Outline each blood parasite and name the species.
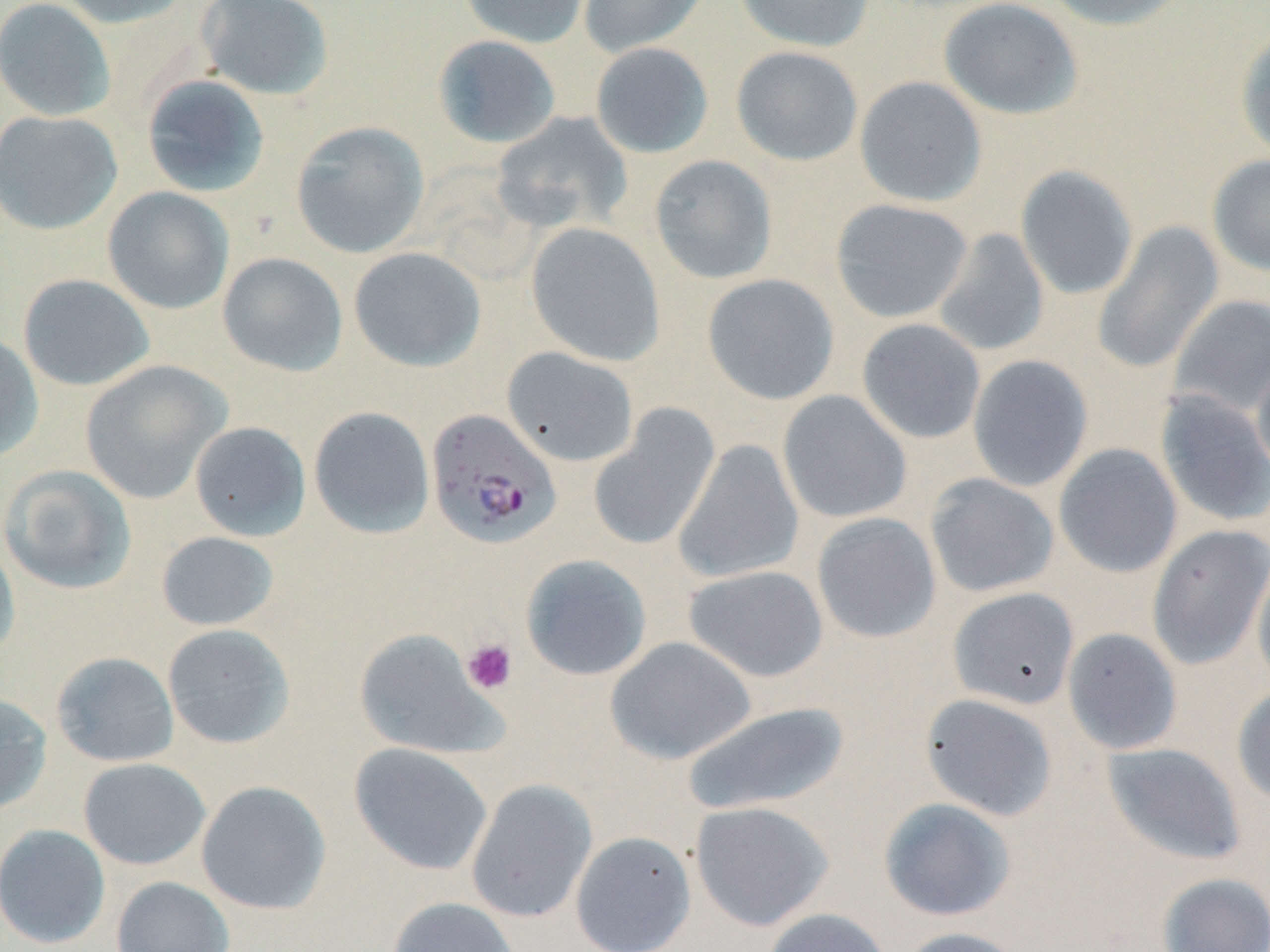

Approximate bounding boxes as (x1, y1, x2, y2) in pixels.
Plasmodium falciparum-infected red blood cells: (426, 409, 562, 549).
No Plasmodium ovale, Plasmodium malariae, Plasmodium vivax, Babesia divergens, or Trypanosoma brucei observed.

Uninfected red blood cell locations: (0, 0, 116, 121), (56, 0, 192, 29), (196, 0, 334, 101), (458, 0, 591, 49), (578, 0, 710, 58), (734, 0, 875, 52), (938, 0, 1084, 120), (1039, 0, 1190, 31), (1235, 26, 1270, 162), (432, 35, 562, 149), (590, 42, 714, 159), (731, 46, 863, 166), (141, 75, 271, 198), (854, 75, 987, 207), (0, 110, 123, 235), (491, 111, 633, 233), (290, 121, 429, 259), (649, 154, 778, 285), (1207, 154, 1270, 276), (1015, 164, 1139, 300), (103, 187, 235, 314), (831, 199, 973, 323), (526, 222, 666, 367), (1092, 222, 1224, 375), (933, 227, 1050, 357), (348, 247, 486, 372), (217, 252, 348, 377), (701, 273, 840, 405), (18, 274, 155, 392), (1169, 294, 1270, 417), (856, 318, 986, 444), (0, 333, 44, 463), (502, 347, 639, 468), (967, 354, 1094, 492), (1252, 356, 1270, 482), (79, 360, 230, 504), (777, 389, 912, 524), (1155, 390, 1270, 527), (589, 405, 721, 552), (308, 406, 435, 539), (190, 421, 312, 542), (673, 439, 804, 584), (1054, 443, 1183, 578), (0, 464, 137, 595), (924, 473, 1060, 598), (811, 512, 942, 644), (1147, 524, 1270, 669), (156, 531, 279, 631), (0, 534, 20, 665), (1252, 553, 1270, 693), (520, 554, 652, 681), (683, 564, 829, 683), (947, 587, 1080, 710), (161, 624, 295, 749), (1062, 627, 1183, 755), (354, 628, 504, 760), (605, 637, 755, 764), (50, 651, 180, 767), (1232, 685, 1270, 806), (0, 692, 52, 815), (920, 693, 1059, 821), (679, 701, 852, 817), (1102, 741, 1246, 867), (349, 742, 494, 876), (78, 758, 211, 870), (465, 779, 598, 923), (196, 780, 332, 915), (878, 797, 1016, 921), (689, 800, 834, 931), (0, 823, 111, 948), (570, 831, 697, 952), (1156, 872, 1270, 952), (111, 876, 235, 952), (386, 896, 522, 952), (760, 907, 895, 952), (896, 926, 1030, 952). Platelet locations: (461, 638, 518, 695). Slide-level diagnosis: Plasmodium falciparum. Captured at 1000x magnification. Thin blood smear. Optical microscopy. One field of a larger specimen. May-Grünwald-Giemsa-stained preparation. Image is 1270×952 pixels.